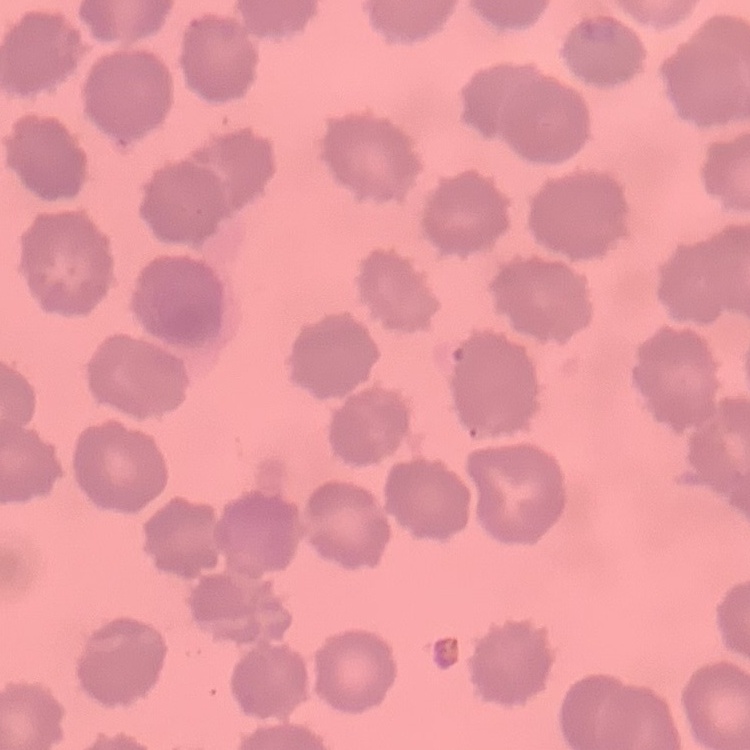
red blood cell morphology = no rouleaux formation
preparation = thin blood film
stain = Field's or Giemsa
image type = one tile cut from a larger photomicrograph